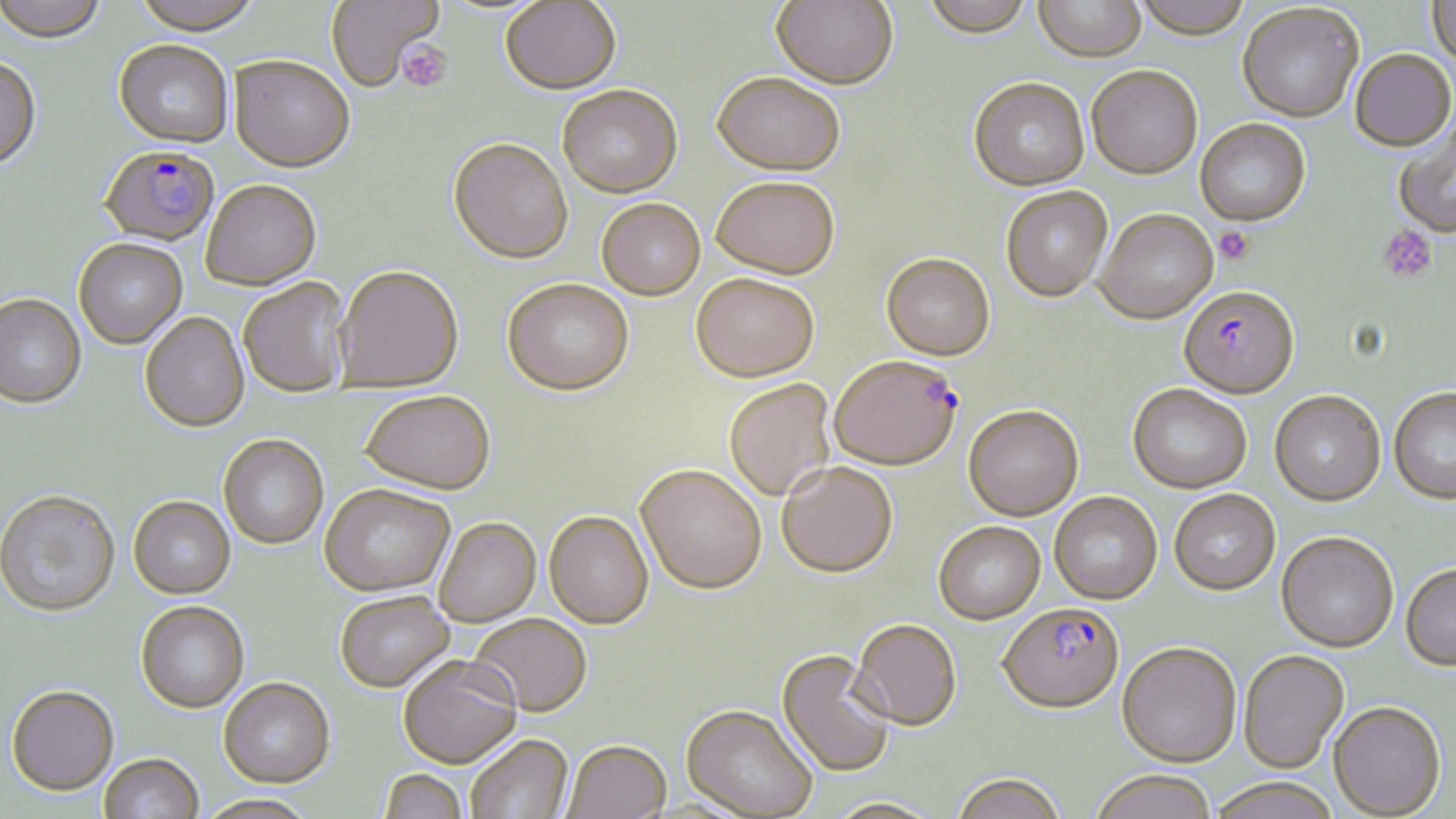
Summary:
  - Coordinate format: approximate bounding boxes as [x1, y1, x2, y2] in pixels
  - Plasmodium falciparum-infected red blood cell locations: [100, 148, 218, 248], [1178, 285, 1299, 398], [830, 354, 962, 470], [998, 602, 1124, 712]
  - Platelet locations: [396, 41, 453, 92], [1377, 225, 1438, 283], [1214, 226, 1255, 265]
  - Uninfected red blood cell locations: [0, 0, 107, 45], [131, 0, 263, 37], [326, 0, 442, 92], [771, 0, 898, 89], [922, 0, 1034, 36], [1132, 0, 1254, 39], [1428, 0, 1456, 67], [500, 1, 621, 95], [1033, 1, 1146, 61], [1237, 3, 1365, 122], [113, 41, 234, 149], [1350, 48, 1455, 151], [230, 57, 354, 175], [0, 59, 42, 173], [1086, 64, 1202, 178], [711, 72, 845, 175], [969, 76, 1090, 189], [557, 85, 683, 198], [1195, 118, 1310, 225], [1393, 121, 1456, 237], [447, 140, 573, 265], [711, 176, 840, 279], [201, 182, 322, 292], [1000, 185, 1113, 301], [596, 198, 705, 301], [1095, 208, 1217, 323], [74, 240, 188, 350], [881, 252, 995, 360], [333, 268, 464, 394], [691, 274, 819, 382], [238, 278, 352, 400], [502, 281, 635, 398], [0, 296, 86, 411], [140, 314, 249, 434], [723, 379, 836, 501], [1128, 382, 1251, 492], [1390, 387, 1456, 502], [1270, 390, 1385, 505], [360, 393, 495, 497], [964, 404, 1083, 519], [218, 436, 328, 550], [776, 461, 898, 577], [636, 466, 766, 594], [320, 488, 455, 599], [1170, 488, 1281, 594], [1049, 491, 1162, 604], [0, 492, 120, 620], [129, 498, 235, 601], [544, 513, 654, 631], [434, 520, 541, 628], [933, 520, 1045, 624], [1276, 531, 1398, 652], [1401, 562, 1456, 669], [335, 594, 455, 694], [135, 602, 249, 714], [468, 616, 592, 719], [850, 618, 962, 729], [1118, 640, 1241, 766], [777, 648, 897, 778], [1238, 648, 1349, 772], [398, 659, 522, 770], [219, 680, 335, 790], [6, 688, 119, 798], [1329, 700, 1446, 818], [681, 705, 818, 817], [466, 736, 573, 819], [563, 741, 671, 819], [99, 754, 204, 819], [1089, 769, 1218, 819], [379, 771, 467, 819], [950, 771, 1067, 819], [1208, 777, 1342, 819], [197, 796, 318, 819], [825, 797, 942, 818]
  - Slide-level diagnosis: Plasmodium falciparum
  - Modality: optical microscopy
  - Field of view: one of a larger specimen
  - Image size: 1456×819 pixels
  - Preparation: thin blood smear
  - Stain: May-Grünwald-Giemsa
  - Magnification: 1000x